Name the blood parasite species.
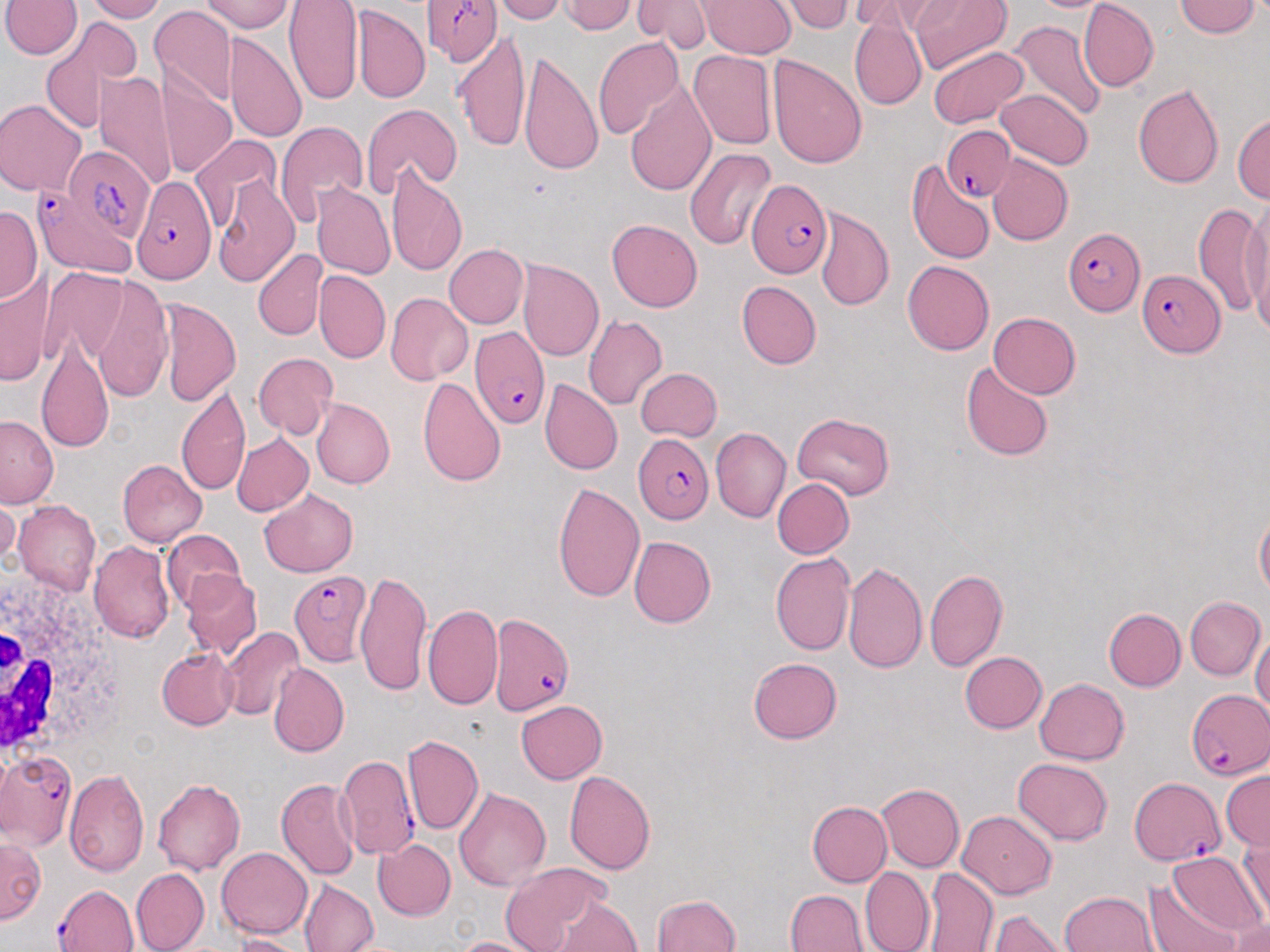
Plasmodium falciparum.

Summary:
  - Coordinate format: approximate bounding boxes as (x1, y1, x2, y2) in pixels
  - White blood cell locations: (0, 561, 124, 766)
  - Plasmodium falciparum-infected red blood cell locations: (426, 0, 501, 68), (941, 131, 1014, 202), (65, 147, 153, 241), (129, 173, 216, 282), (745, 178, 830, 280), (34, 196, 135, 272), (1060, 225, 1146, 314), (1137, 267, 1225, 357), (472, 329, 550, 427), (634, 432, 717, 522), (287, 570, 372, 664), (489, 613, 576, 718), (1186, 688, 1268, 778), (2, 750, 77, 849), (335, 754, 420, 861), (1128, 777, 1228, 867), (54, 882, 139, 952)
  - Uninfected red blood cell locations: (3, 0, 81, 61), (82, 0, 164, 22), (203, 0, 295, 31), (287, 0, 360, 104), (496, 0, 569, 23), (562, 0, 636, 36), (633, 0, 709, 52), (703, 0, 795, 58), (784, 0, 852, 33), (910, 0, 1010, 75), (1032, 0, 1105, 15), (1078, 0, 1158, 88), (1176, 0, 1261, 39), (852, 2, 923, 38), (151, 10, 236, 108), (354, 10, 429, 105), (1010, 19, 1106, 119), (849, 20, 925, 108), (37, 22, 136, 134), (456, 29, 530, 151), (227, 34, 306, 144), (594, 37, 683, 135), (929, 43, 1027, 126), (689, 50, 777, 149), (519, 51, 604, 173), (768, 54, 868, 168), (157, 70, 237, 178), (98, 72, 176, 195), (626, 77, 717, 198), (1133, 82, 1225, 188), (995, 89, 1091, 170), (0, 98, 85, 197), (358, 103, 461, 200), (1233, 108, 1270, 209), (274, 118, 367, 231), (191, 133, 282, 232), (684, 145, 777, 249), (986, 158, 1072, 245), (906, 161, 995, 266), (388, 164, 466, 275), (211, 175, 298, 285), (314, 185, 395, 282), (1238, 198, 1270, 328), (1196, 200, 1267, 322), (0, 204, 41, 301), (815, 210, 894, 311), (607, 220, 702, 311), (442, 244, 526, 329), (253, 248, 325, 339), (901, 260, 994, 356), (519, 262, 604, 364), (3, 268, 55, 388), (316, 271, 390, 363), (82, 275, 174, 400), (739, 280, 822, 368), (385, 293, 471, 385), (157, 299, 241, 407), (37, 308, 117, 458), (990, 311, 1082, 398), (585, 313, 667, 410), (252, 352, 337, 441), (963, 359, 1053, 462), (634, 368, 721, 440), (418, 376, 507, 486), (540, 377, 621, 476), (175, 384, 251, 500), (313, 399, 394, 488), (790, 413, 901, 498), (0, 416, 61, 509), (712, 428, 791, 522), (232, 432, 313, 517), (118, 461, 207, 547), (773, 478, 853, 559), (550, 481, 644, 601), (261, 488, 358, 577), (1, 498, 19, 573), (13, 502, 101, 597), (1254, 508, 1268, 600), (158, 530, 245, 612), (628, 534, 717, 628), (90, 538, 175, 643), (770, 551, 854, 655), (842, 559, 929, 674), (924, 568, 1007, 670), (180, 569, 261, 657), (356, 569, 431, 698), (1185, 597, 1265, 680), (423, 602, 504, 710), (1105, 606, 1185, 690), (221, 629, 303, 722), (1251, 629, 1269, 724), (156, 647, 237, 729), (961, 650, 1048, 734), (744, 655, 845, 744), (268, 663, 349, 758), (1033, 677, 1130, 765), (515, 699, 608, 784), (401, 733, 482, 835), (1013, 756, 1113, 845), (564, 770, 656, 875), (65, 771, 149, 877), (1220, 771, 1270, 846), (153, 777, 247, 873), (276, 779, 361, 878), (877, 782, 964, 873), (453, 787, 551, 891), (806, 800, 891, 886), (957, 811, 1060, 898), (1236, 830, 1270, 921), (0, 838, 43, 925), (375, 839, 458, 920), (215, 846, 312, 939), (1165, 851, 1265, 941), (498, 860, 615, 950), (233, 863, 377, 944), (860, 868, 933, 952), (920, 868, 996, 952), (130, 869, 208, 950), (1142, 878, 1250, 952), (299, 880, 377, 952), (787, 887, 871, 952), (1057, 890, 1156, 952), (652, 891, 742, 952), (550, 893, 642, 951), (987, 909, 1064, 952), (1223, 914, 1270, 952), (229, 932, 302, 952), (451, 933, 537, 952)
  - Field of view: single
  - Preparation: thin blood smear
  - Modality: optical microscopy
  - Image size: 1270×952 pixels
  - Stain: May-Grünwald-Giemsa
  - Magnification: 1000x